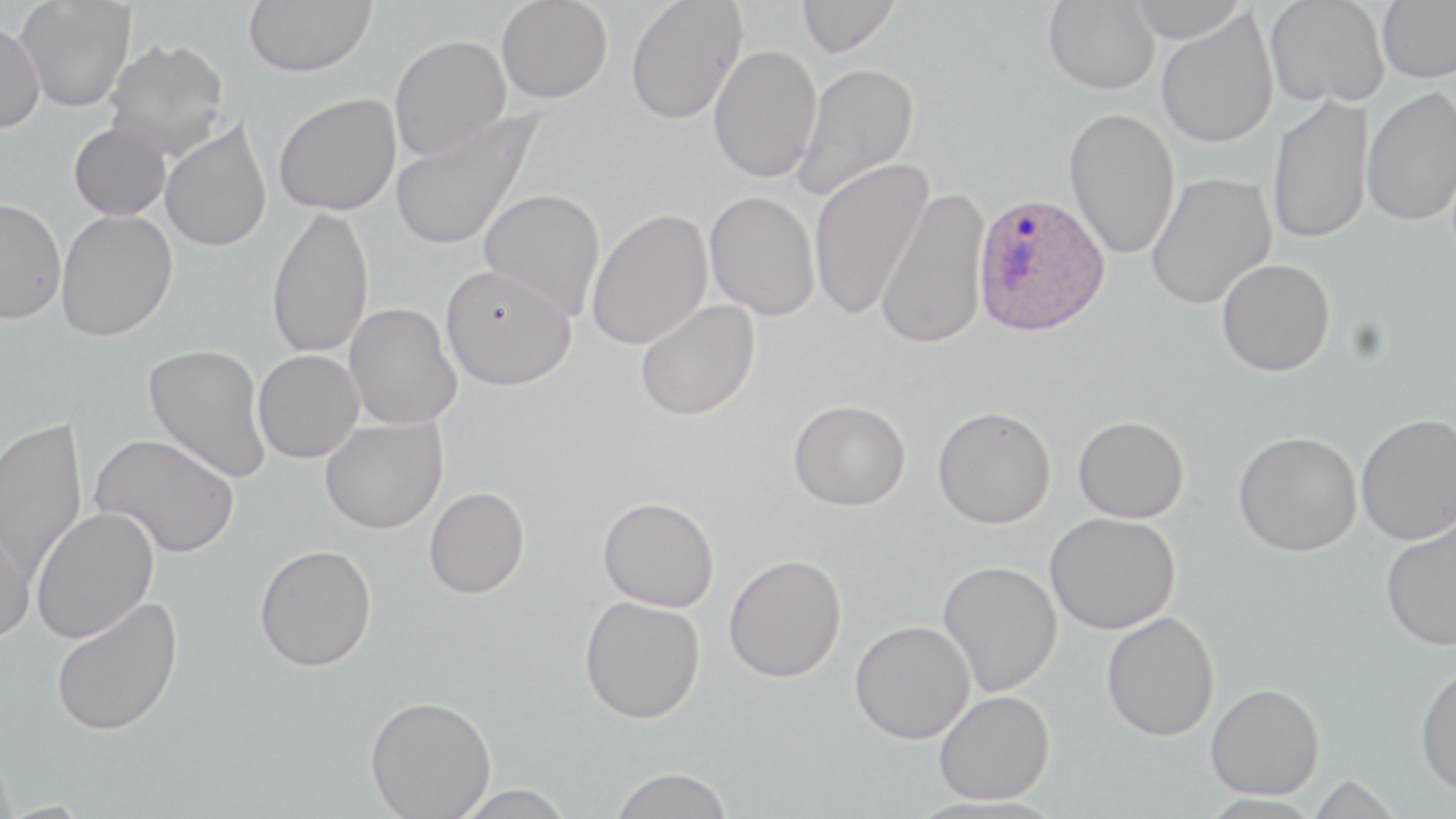

Approximate bounding boxes as (x1,y1)-(x2,y2) corner pairs in pixels. Uninfected red blood cell locations: (14,0)-(136,113), (243,0)-(376,77), (496,0)-(612,103), (625,0)-(747,124), (797,0)-(901,57), (1044,0)-(1160,94), (1124,0)-(1247,42), (1265,0)-(1389,108), (1377,1)-(1456,83), (1156,10)-(1279,148), (0,21)-(45,134), (389,35)-(511,160), (104,39)-(230,160), (709,44)-(822,183), (792,62)-(920,201), (1361,86)-(1456,226), (274,92)-(401,215), (1267,94)-(1375,245), (390,108)-(545,253), (1064,108)-(1180,260), (160,119)-(272,253), (69,122)-(171,221), (808,157)-(934,321), (1146,172)-(1276,308), (479,188)-(606,321), (876,188)-(990,350), (704,190)-(820,320), (0,197)-(66,324), (266,205)-(374,360), (586,208)-(713,351), (56,210)-(178,341), (1216,258)-(1335,376), (440,263)-(576,390), (635,299)-(760,421), (344,303)-(461,429), (144,343)-(272,484), (253,349)-(365,463), (788,399)-(910,510), (932,406)-(1056,529), (1355,413)-(1456,545), (1073,415)-(1189,523), (0,417)-(87,583), (320,417)-(447,533), (1233,431)-(1362,556), (91,433)-(240,557), (424,487)-(530,599), (598,496)-(719,611), (31,507)-(159,643), (1045,512)-(1180,634), (1379,514)-(1456,651), (0,520)-(35,645), (254,544)-(377,671), (724,553)-(847,682), (938,560)-(1062,697), (579,595)-(705,723), (51,596)-(183,737), (1101,611)-(1220,741), (850,620)-(975,743), (1415,664)-(1456,796), (1206,683)-(1324,799), (933,689)-(1054,804), (365,695)-(495,819), (609,767)-(733,819). Plasmodium ovale-infected red blood cell locations: (973,192)-(1110,337). Slide-level diagnosis: Plasmodium ovale. Thin blood film. Captured at 1000x magnification. Image is 1456×819 pixels. May-Grünwald-Giemsa-stained preparation. One field of a larger specimen. Optical microscopy.